Comment on the morphology of the red blood cells.
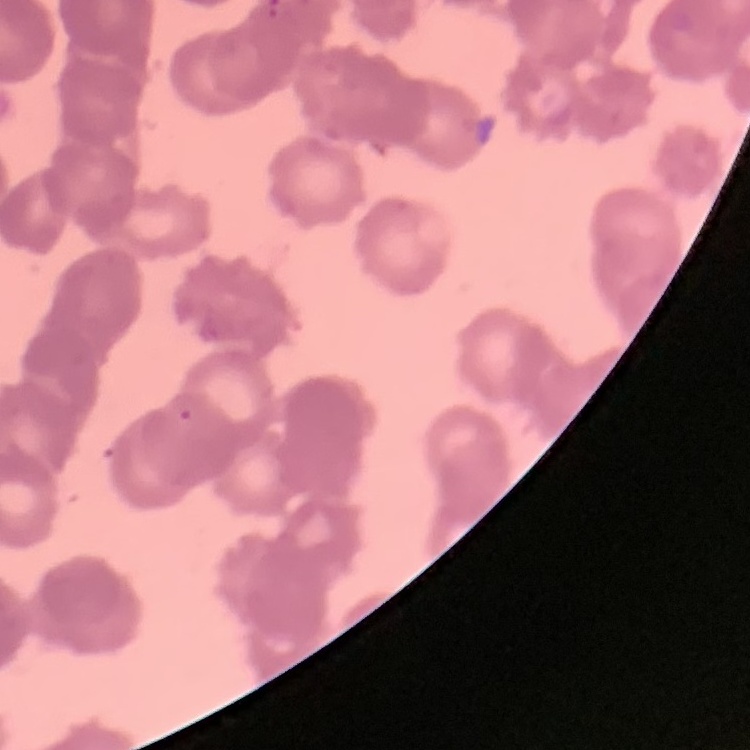
They show rouleaux formation.

Summary:
  - Stain: Field's or Giemsa
  - Image type: one tile cut from a larger photomicrograph
  - Preparation: thin blood smear